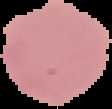
{
  "preparation": "thin blood smear",
  "image_size": "112×109 pixels",
  "image_type": "cell region segmented out of the field of view; surrounding area masked to black",
  "malaria_status": "uninfected"
}